Assess for malaria.
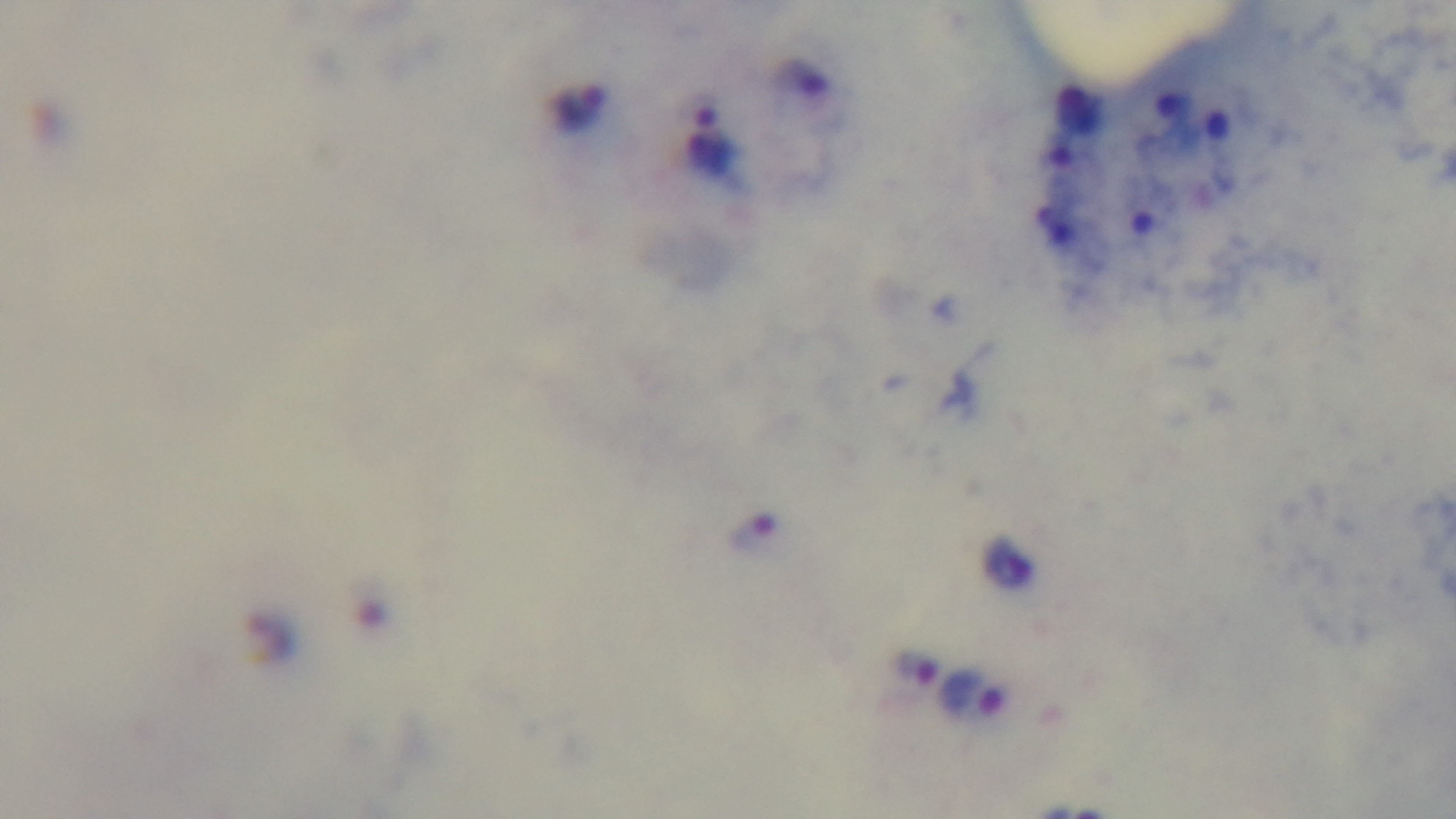

It is infected.

Summary:
  - Capture: mounted 4K digital camera
  - Modality: light microscopy
  - Preparation: thick
  - Objective: 100x oil immersion
  - Field of view: one from the slide
  - Stain: Giemsa